Name the parasite shown.
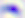
This is Toxoplasma gondii.

Summary:
  - Modality: micrograph
  - Magnification: 400x